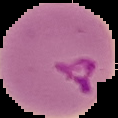
{
  "result": "Plasmodium parasites detected",
  "preparation": "thin blood film",
  "image_size": "118×118 pixels",
  "image_type": "cell region segmented out of the field of view; surrounding area masked to black"
}